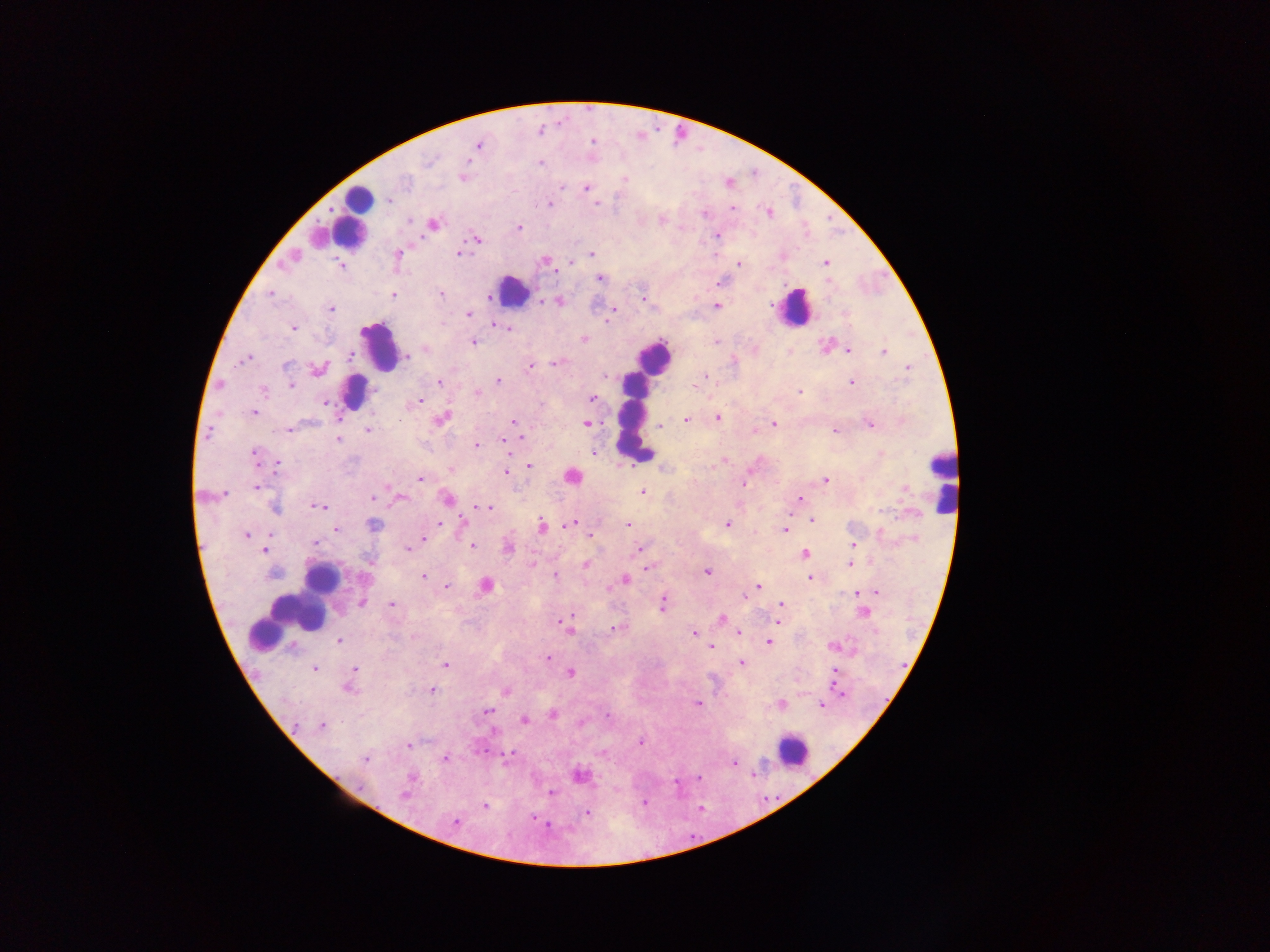
Approximate centers as [x, y] in pixels.
Summary:
  - Plasmodium parasite locations: [478, 145], [429, 161], [540, 163], [465, 175], [624, 179], [562, 187], [586, 188], [389, 200], [549, 204], [598, 204], [733, 209], [768, 213], [703, 214], [409, 221], [661, 221], [433, 224], [519, 227], [717, 235], [477, 239], [459, 253], [591, 254], [397, 255], [292, 257], [545, 261], [571, 263], [826, 263], [739, 264], [341, 265], [600, 278], [721, 282], [270, 293], [441, 294], [393, 295], [489, 299], [645, 300], [559, 302], [716, 306], [331, 309], [614, 310], [468, 314], [611, 314], [496, 323], [501, 326], [507, 327], [293, 328], [584, 339], [473, 342], [715, 342], [425, 349], [849, 351], [883, 351], [350, 355], [407, 356], [246, 359], [554, 363], [287, 365], [530, 366], [908, 367], [318, 370], [606, 376], [705, 376], [498, 381], [440, 382], [851, 382], [698, 383], [291, 384], [694, 387], [263, 390], [376, 391], [799, 391], [477, 393], [592, 398], [419, 402], [325, 403], [254, 413], [717, 417], [442, 418], [685, 420], [513, 422], [586, 424], [775, 424], [870, 424], [662, 425], [289, 429], [368, 430], [754, 430], [835, 430], [209, 433], [522, 437], [339, 438], [503, 440], [476, 445], [593, 452], [254, 453], [881, 453], [278, 463], [529, 465], [714, 466], [451, 469], [505, 474], [572, 476], [420, 479], [825, 480], [744, 482], [256, 487], [642, 492], [224, 493], [202, 497], [373, 498], [399, 498], [446, 498], [799, 499], [317, 507], [488, 507], [274, 508], [813, 520], [463, 521], [573, 523], [439, 524], [628, 524], [727, 524], [374, 525], [543, 526], [336, 530], [784, 530], [270, 534], [247, 535], [590, 536], [423, 540], [315, 543], [854, 544], [472, 546], [509, 547], [409, 548], [638, 549], [264, 550], [805, 554], [532, 564], [850, 564], [586, 565], [648, 567], [707, 571], [274, 574], [556, 576], [423, 577], [810, 578], [624, 579], [486, 585], [757, 586], [447, 587], [856, 593], [876, 593], [744, 596], [362, 603], [392, 604], [663, 604], [781, 604], [864, 613], [722, 618], [563, 621], [778, 622], [615, 627], [567, 628], [693, 633], [739, 633], [414, 637], [339, 640], [769, 642], [833, 647], [712, 648], [547, 658], [741, 662], [445, 665], [355, 668], [315, 669], [835, 671], [571, 673], [353, 675], [349, 688], [431, 689], [506, 691], [838, 691], [699, 704], [781, 704], [821, 706], [487, 711], [553, 715], [607, 715], [525, 720], [321, 727], [640, 743], [408, 745], [508, 755], [365, 759], [445, 759], [733, 762], [580, 776], [411, 778], [550, 793], [404, 795], [485, 806], [586, 813], [535, 819], [454, 823], [546, 825]
  - Leukocyte locations: [353, 215], [318, 238], [513, 291], [794, 307], [379, 347], [652, 359], [353, 389], [634, 424], [941, 478], [321, 578], [298, 611], [264, 624], [793, 750]
  - Image size: 1270×952 pixels
  - Preparation: thick blood film
  - Country: Ghana
  - Capture: mobile-phone photograph through a microscope
  - Field of view: single